Describe the morphology of the erythrocytes.
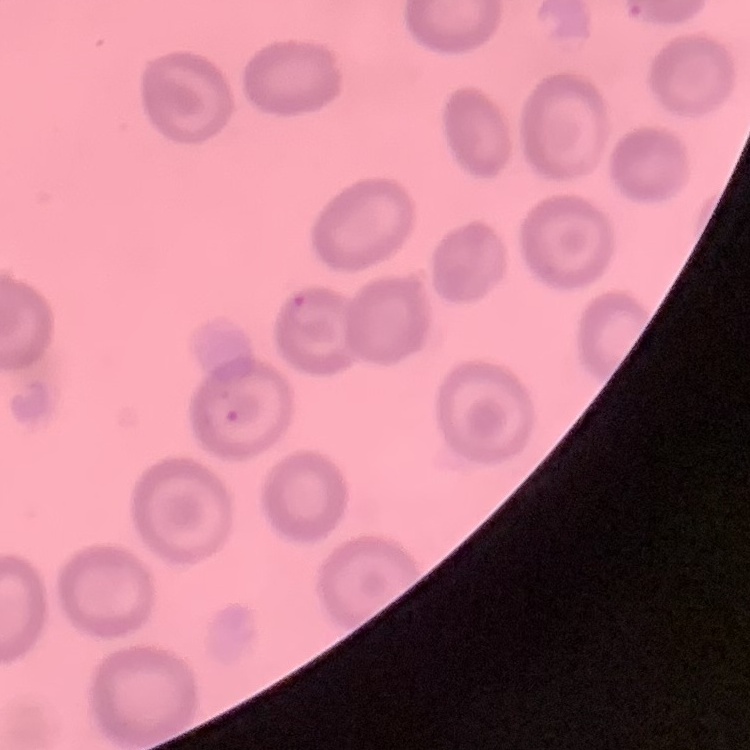

They show no rouleaux formation.

stain: Field's or Giemsa
preparation: thin blood film
image_type: one tile cut from a larger photomicrograph